Outline each Plasmodium falciparum-infected red blood cell.
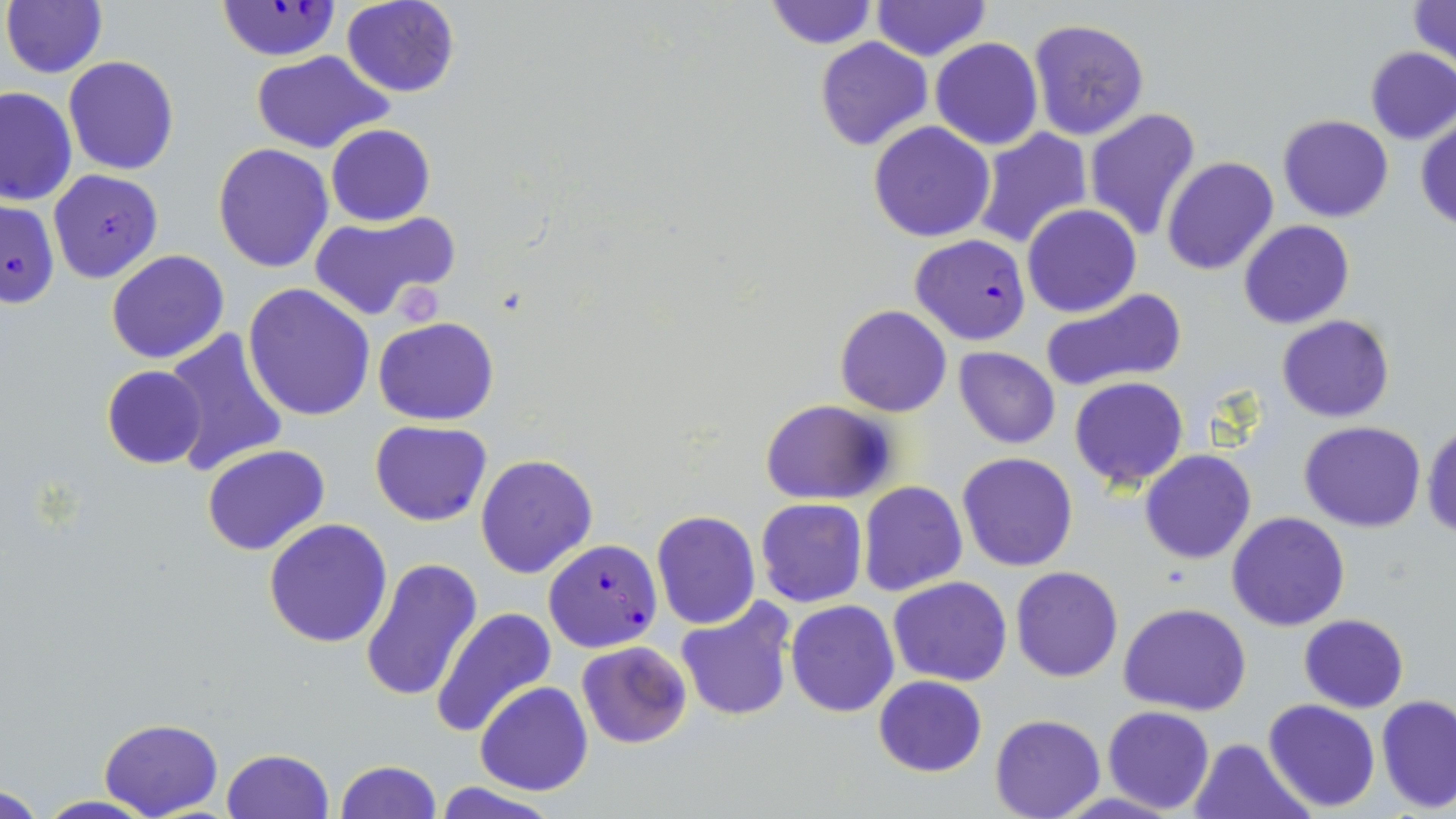
Approximate bounding boxes as (x1, y1, x2, y2) in pixels.
Plasmodium falciparum-infected red blood cells: (217, 3, 338, 60), (48, 169, 163, 284), (0, 198, 60, 311), (909, 233, 1033, 346), (543, 539, 662, 651).

Platelet locations: (395, 286, 442, 328). Uninfected red blood cell locations: (341, 0, 461, 97), (873, 0, 988, 61), (1406, 0, 1455, 67), (763, 1, 876, 48), (3, 2, 107, 78), (1026, 17, 1150, 141), (814, 38, 933, 152), (931, 38, 1043, 150), (926, 40, 1057, 247), (1366, 48, 1456, 144), (248, 50, 394, 155), (63, 56, 179, 175), (0, 85, 76, 206), (1084, 107, 1202, 241), (1277, 115, 1394, 222), (1416, 117, 1456, 231), (869, 119, 997, 241), (326, 123, 436, 227), (970, 128, 1093, 250), (213, 144, 334, 273), (1162, 155, 1279, 276), (1022, 204, 1141, 318), (308, 210, 461, 323), (1238, 220, 1355, 330), (106, 249, 231, 364), (121, 258, 267, 422), (243, 284, 375, 421), (1040, 288, 1188, 393), (835, 304, 953, 417), (1278, 315, 1394, 422), (373, 317, 500, 424), (163, 329, 290, 477), (953, 346, 1060, 449), (101, 364, 208, 469), (1069, 376, 1189, 490), (758, 398, 898, 505), (370, 420, 492, 526), (1299, 421, 1426, 532), (1423, 422, 1456, 539), (201, 444, 330, 556), (1139, 449, 1255, 564), (955, 452, 1078, 573), (476, 453, 598, 578), (857, 481, 967, 596), (755, 498, 867, 607), (650, 509, 760, 630), (1226, 512, 1350, 631), (263, 518, 394, 649), (360, 557, 483, 703), (1011, 566, 1123, 682), (889, 576, 1012, 686), (675, 598, 797, 723), (785, 599, 900, 718), (1120, 603, 1251, 716), (431, 607, 557, 736), (1299, 614, 1407, 712), (576, 640, 692, 748), (872, 674, 988, 777), (476, 682, 592, 796), (1378, 694, 1456, 812), (1262, 699, 1381, 813), (1103, 706, 1215, 813), (990, 714, 1105, 819), (98, 718, 222, 818), (1189, 737, 1310, 819), (221, 748, 335, 819), (333, 760, 441, 818), (432, 782, 560, 819), (1, 783, 52, 817), (31, 796, 163, 819). Slide-level diagnosis: Plasmodium falciparum. Optical microscopy. One field of a larger specimen. Image is 1456×819 pixels. Thin blood smear. May-Grünwald-Giemsa stain. Captured at 1000x magnification.